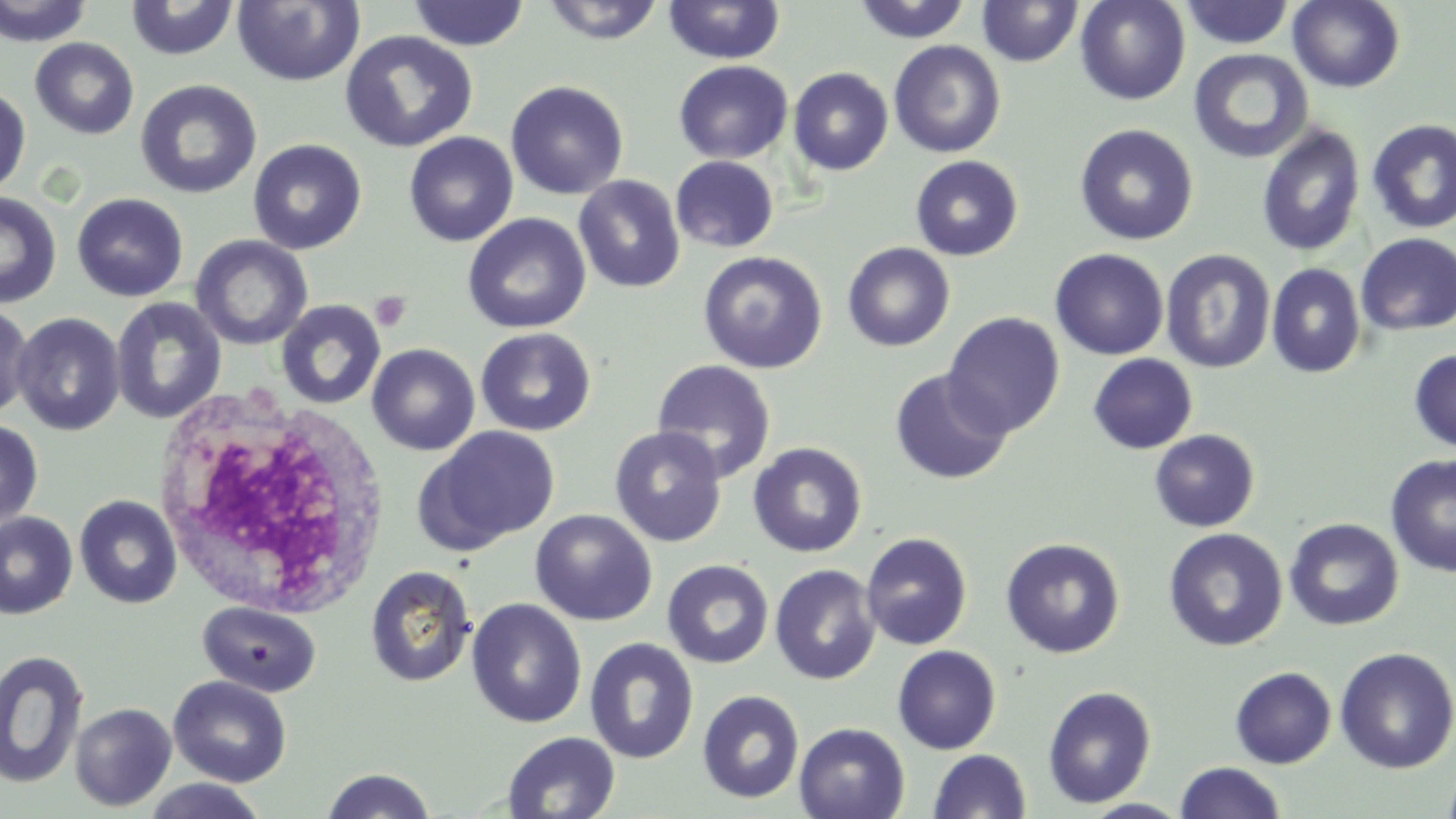

Summary:
  - Coordinate format: approximate bounding boxes as named x1/y1/x2/y2 corners in pixels
  - Platelet locations: (x1=370, y1=291, x2=411, y2=332)
  - White blood cell locations: (x1=156, y1=391, x2=393, y2=619)
  - Uninfected red blood cell locations: (x1=0, y1=0, x2=95, y2=46), (x1=540, y1=0, x2=667, y2=45), (x1=852, y1=0, x2=973, y2=44), (x1=1075, y1=0, x2=1191, y2=105), (x1=1288, y1=0, x2=1405, y2=93), (x1=125, y1=1, x2=240, y2=61), (x1=232, y1=1, x2=365, y2=87), (x1=407, y1=1, x2=530, y2=50), (x1=663, y1=1, x2=786, y2=65), (x1=977, y1=1, x2=1083, y2=67), (x1=1179, y1=1, x2=1295, y2=50), (x1=340, y1=30, x2=478, y2=153), (x1=30, y1=37, x2=139, y2=140), (x1=888, y1=39, x2=1006, y2=158), (x1=1188, y1=48, x2=1313, y2=164), (x1=673, y1=61, x2=794, y2=164), (x1=788, y1=67, x2=893, y2=175), (x1=134, y1=79, x2=263, y2=199), (x1=505, y1=80, x2=628, y2=200), (x1=0, y1=87, x2=30, y2=196), (x1=1367, y1=119, x2=1456, y2=233), (x1=1074, y1=123, x2=1199, y2=246), (x1=1256, y1=123, x2=1366, y2=258), (x1=403, y1=132, x2=519, y2=247), (x1=247, y1=138, x2=367, y2=255), (x1=671, y1=155, x2=779, y2=253), (x1=910, y1=155, x2=1023, y2=261), (x1=573, y1=175, x2=686, y2=293), (x1=0, y1=192, x2=61, y2=308), (x1=72, y1=193, x2=189, y2=302), (x1=463, y1=213, x2=591, y2=334), (x1=1356, y1=233, x2=1455, y2=335), (x1=191, y1=235, x2=312, y2=350), (x1=842, y1=242, x2=955, y2=352), (x1=1050, y1=249, x2=1169, y2=360), (x1=1160, y1=249, x2=1276, y2=373), (x1=698, y1=250, x2=828, y2=373), (x1=1266, y1=263, x2=1366, y2=378), (x1=111, y1=297, x2=227, y2=424), (x1=276, y1=299, x2=386, y2=410), (x1=0, y1=302, x2=34, y2=419), (x1=943, y1=312, x2=1065, y2=438), (x1=11, y1=313, x2=125, y2=436), (x1=475, y1=327, x2=597, y2=436), (x1=367, y1=344, x2=480, y2=455), (x1=1409, y1=349, x2=1456, y2=453), (x1=1088, y1=353, x2=1198, y2=454), (x1=652, y1=360, x2=777, y2=483), (x1=889, y1=369, x2=1014, y2=485), (x1=0, y1=419, x2=43, y2=530), (x1=609, y1=425, x2=727, y2=547), (x1=419, y1=426, x2=561, y2=552), (x1=1150, y1=429, x2=1260, y2=532), (x1=747, y1=442, x2=867, y2=558), (x1=1385, y1=453, x2=1456, y2=577), (x1=74, y1=494, x2=183, y2=609), (x1=530, y1=509, x2=657, y2=626), (x1=0, y1=512, x2=78, y2=619), (x1=1284, y1=517, x2=1404, y2=630), (x1=1164, y1=528, x2=1288, y2=651), (x1=860, y1=533, x2=972, y2=650), (x1=1000, y1=536, x2=1126, y2=659), (x1=662, y1=559, x2=774, y2=669), (x1=769, y1=564, x2=881, y2=685), (x1=365, y1=565, x2=477, y2=688), (x1=466, y1=598, x2=587, y2=728), (x1=197, y1=600, x2=321, y2=697), (x1=585, y1=638, x2=699, y2=764), (x1=892, y1=644, x2=1001, y2=754), (x1=1334, y1=647, x2=1456, y2=774), (x1=0, y1=650, x2=89, y2=789), (x1=1230, y1=666, x2=1337, y2=768), (x1=168, y1=675, x2=292, y2=787), (x1=1042, y1=685, x2=1157, y2=808), (x1=697, y1=690, x2=805, y2=804), (x1=70, y1=703, x2=177, y2=811), (x1=794, y1=722, x2=910, y2=819), (x1=502, y1=732, x2=621, y2=818), (x1=928, y1=749, x2=1032, y2=819), (x1=1441, y1=758, x2=1456, y2=819), (x1=1174, y1=761, x2=1287, y2=818), (x1=321, y1=768, x2=437, y2=819), (x1=140, y1=778, x2=270, y2=818)
  - Slide-level diagnosis: negative for blood parasites
  - Preparation: thin blood smear
  - Modality: light microscopy
  - Field of view: single
  - Image size: 1456×819 pixels
  - Stain: May-Grünwald-Giemsa
  - Magnification: 1000x